Report the malaria status of this cell.
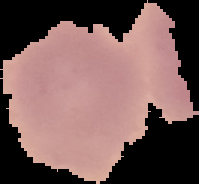
Uninfected.

image type = segmented cell region on a black background
image size = 199×184 pixels
preparation = thin blood smear